Point out each Plasmodium parasite.
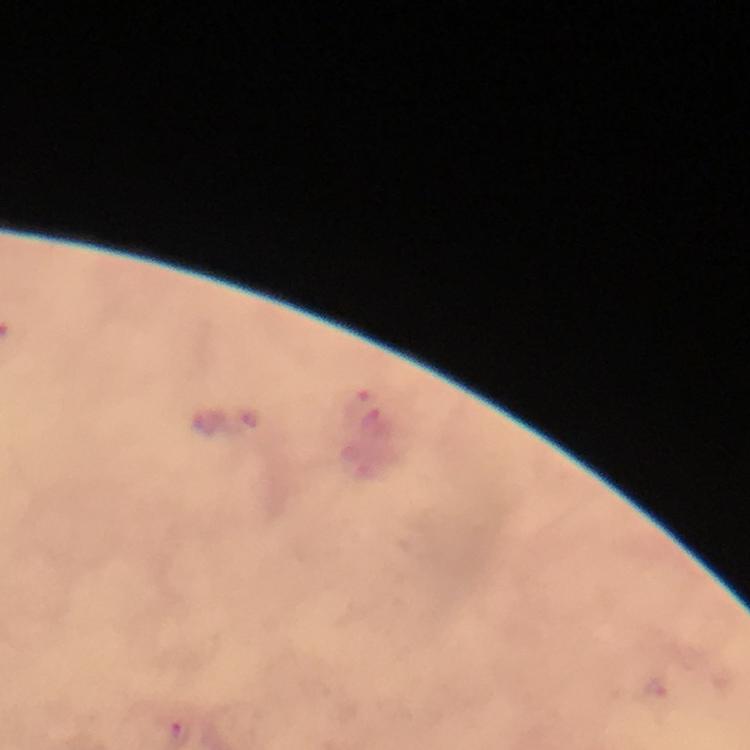

Approximate object centers, in pixels from the top-left corner.
Plasmodium parasites: (x=362, y=403).

{
  "immersion_oil": "applied",
  "stain": "Giemsa",
  "magnification": "100x",
  "context": "from a diagnostic examination for malaria",
  "preparation": "thick smear",
  "image_size": "750×750 pixels",
  "capture": "smartphone photograph through a microscope",
  "cropped_from": "one field of view"
}